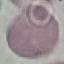
Summary:
  - Malaria status: uninfected
  - Preparation: thin smear
  - Stain: Giemsa
  - Image type: automatically extracted cell patch, resized to 64 × 64 pixels
  - Capture: smartphone camera at the microscope eyepiece